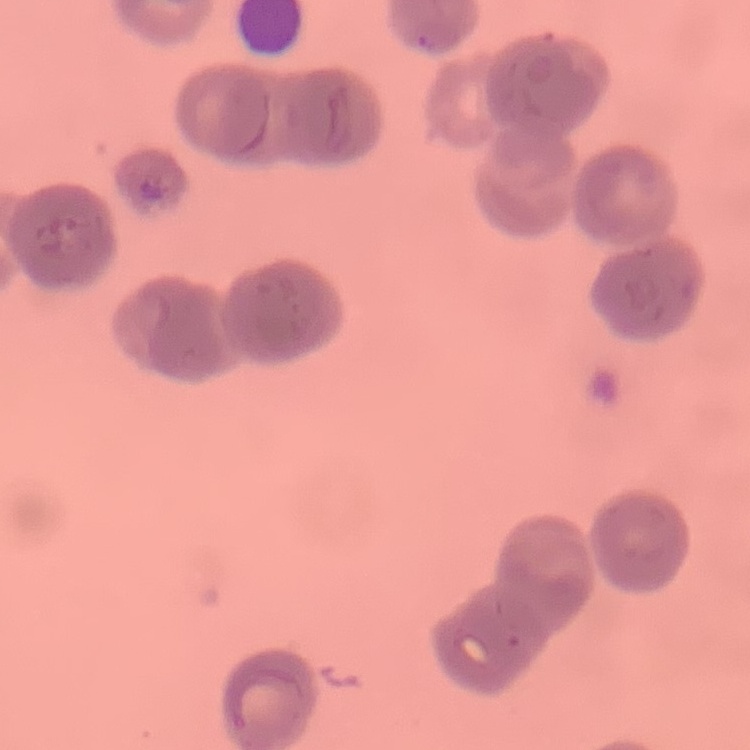
erythrocyte morphology = rouleaux formation
image type = square crop of a larger photomicrograph
stain = Field's or Giemsa
preparation = thin blood smear